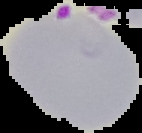 Result: Plasmodium parasites detected. From a thin blood smear. Cell region segmented out of the field of view; the surrounding area is masked to black. Image is 142×133 pixels.